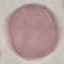
Result: no malaria parasites seen. Giemsa stain. Acquired by smartphone through the microscope eyepiece. Cell patch, automatically extracted from a larger field of view and resized to 64 × 64 pixels. Thin smear of blood.